Give the position of every leukocyte visible.
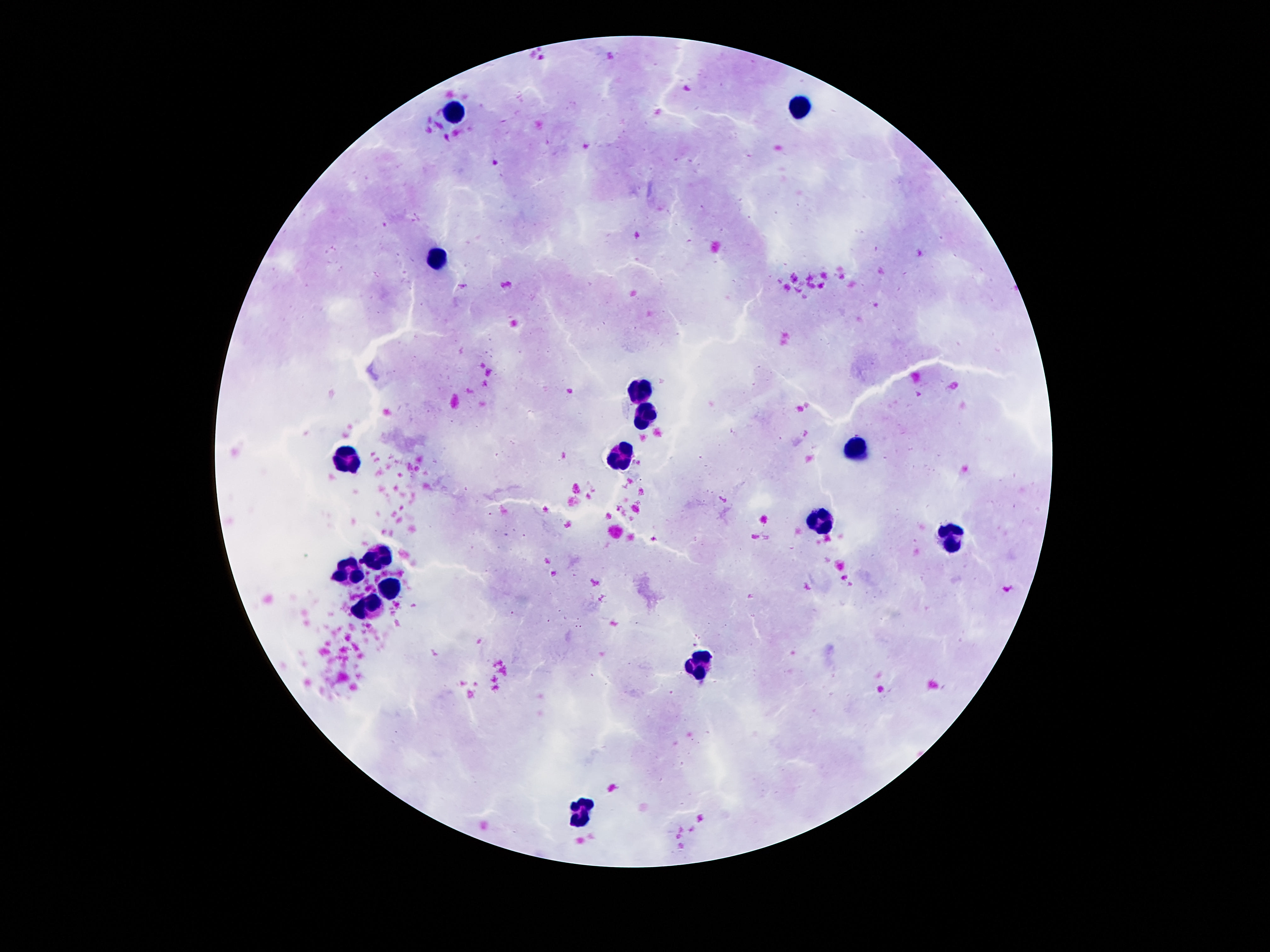
Approximate centers as {x, y} in pixels.
Leukocytes: {796, 100}, {457, 113}, {434, 258}, {641, 391}, {644, 415}, {854, 449}, {621, 452}, {347, 459}, {818, 520}, {954, 539}, {379, 555}, {347, 572}, {389, 591}, {366, 607}, {699, 664}, {579, 814}.

field of view = one from this slide
magnification = 100x
capture = smartphone camera through the microscope eyepiece
stain = Giemsa
preparation = thick blood smear
image size = 1270×952 pixels
patient malaria status = negative